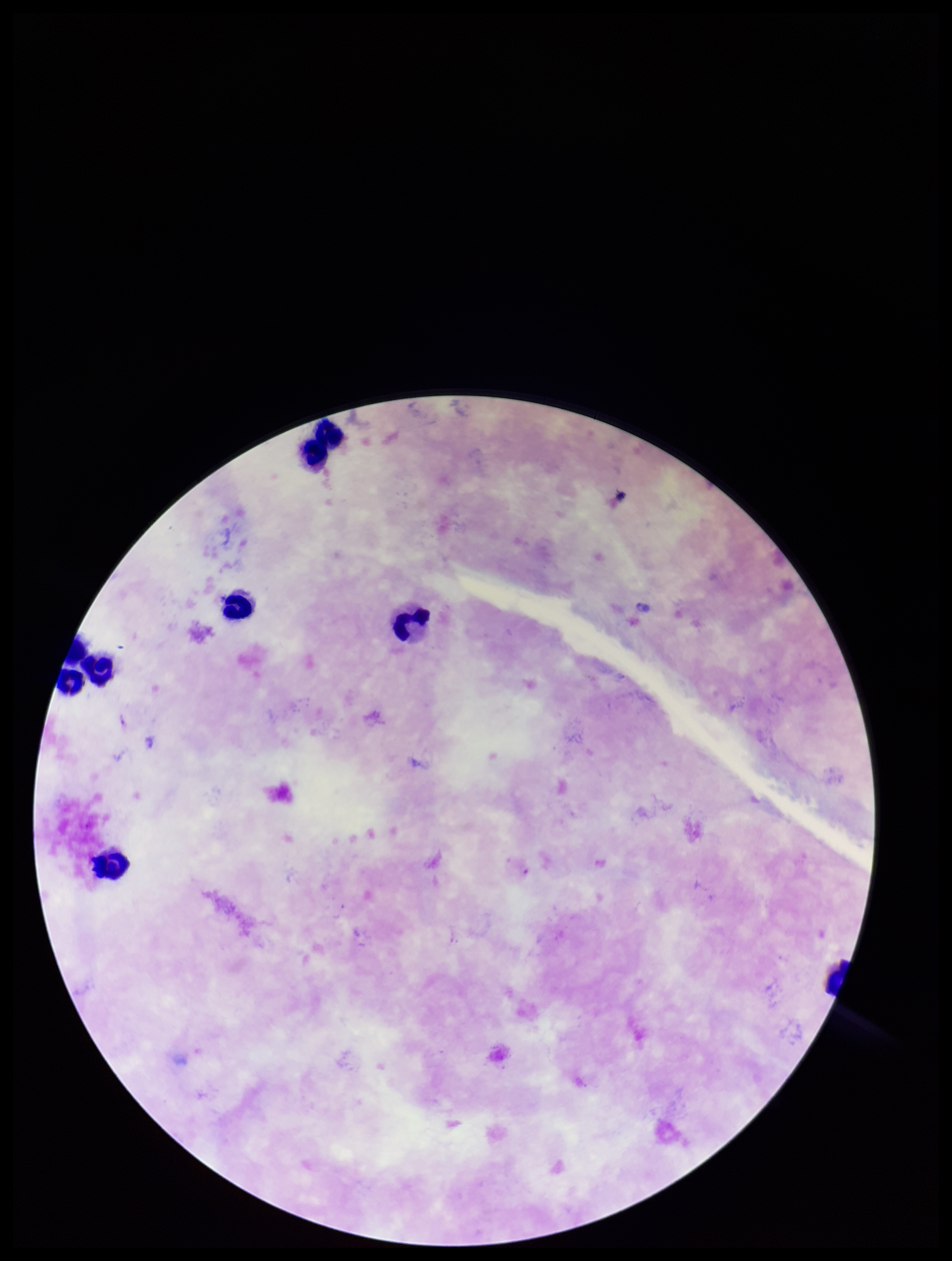

Summary:
  - Stain: Giemsa
  - Patient malaria status: positive
  - Parasite count: 0
  - Capture: smartphone photograph through the microscope eyepiece
  - Leukocyte count: 7
  - Plasmodium parasites: none detected
  - Image size: 952×1261 pixels
  - Preparation: thick blood smear
  - Field of view: single
  - Species reported for this patient: Plasmodium falciparum